Comment on the morphology of the erythrocytes.
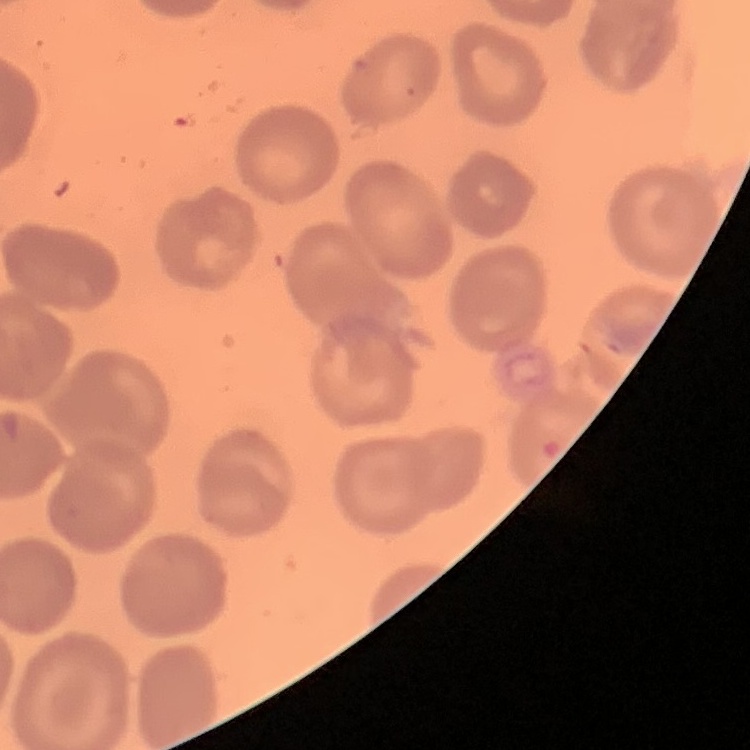

No rouleaux formation.

Square crop of a larger photomicrograph. Thin blood smear. Stained with either Field's or Giemsa.